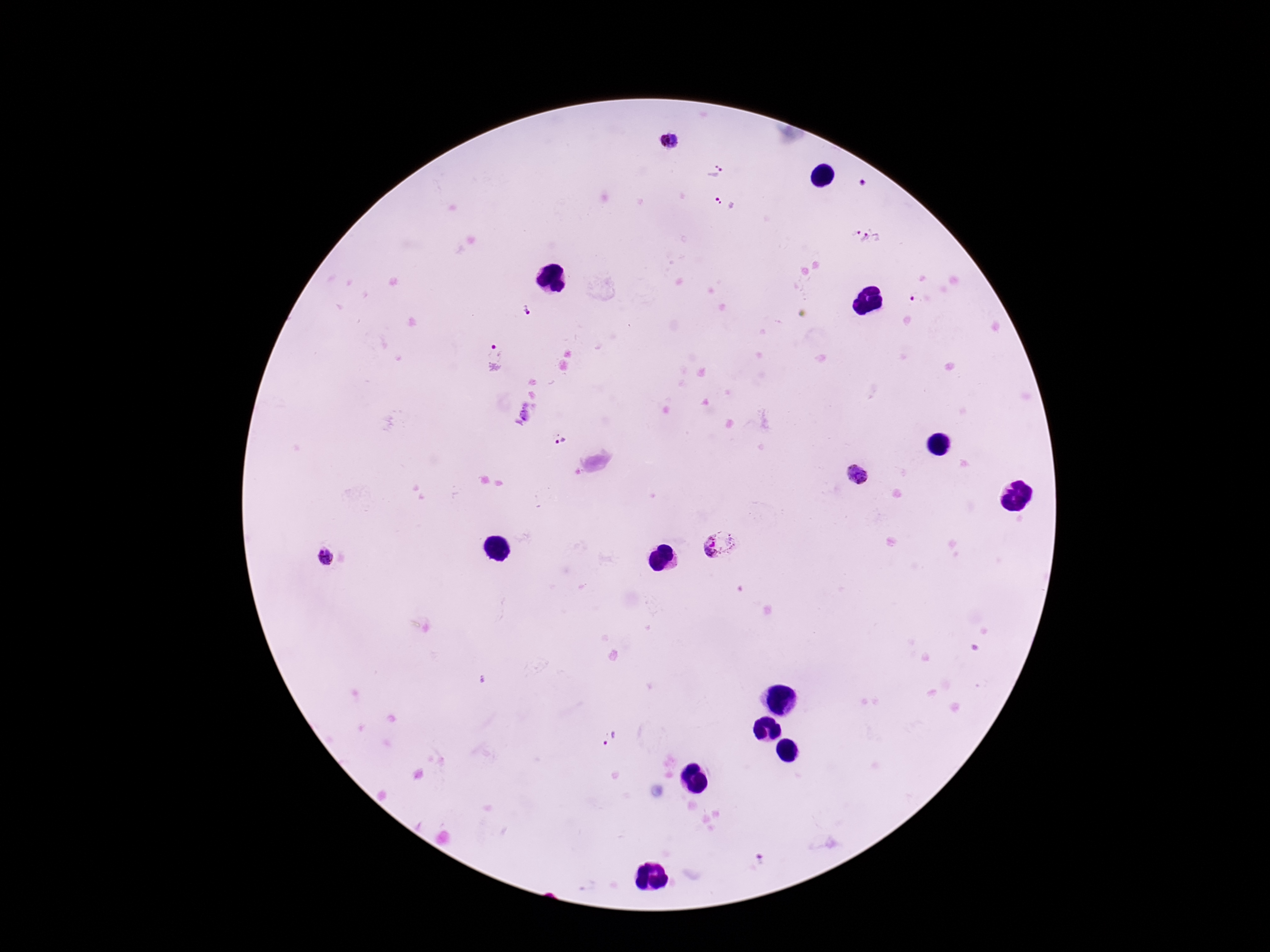

capture: smartphone camera through the microscope eyepiece
magnification: 100x
stain: Giemsa
image_size: 1270×952 pixels
plasmodium_parasite_locations: 'approximate object centers, in pixels from the top-left corner: (x=671, y=140), (x=716, y=170), (x=862, y=184), (x=724, y=202), (x=865, y=234), (x=913, y=297), (x=526, y=311), (x=495, y=350), (x=559, y=438), (x=856, y=473), (x=719, y=543), (x=327, y=558), (x=609, y=737), (x=757, y=860)'
patient_malaria_status: positive
field_of_view: one from this slide
preparation: thick blood film